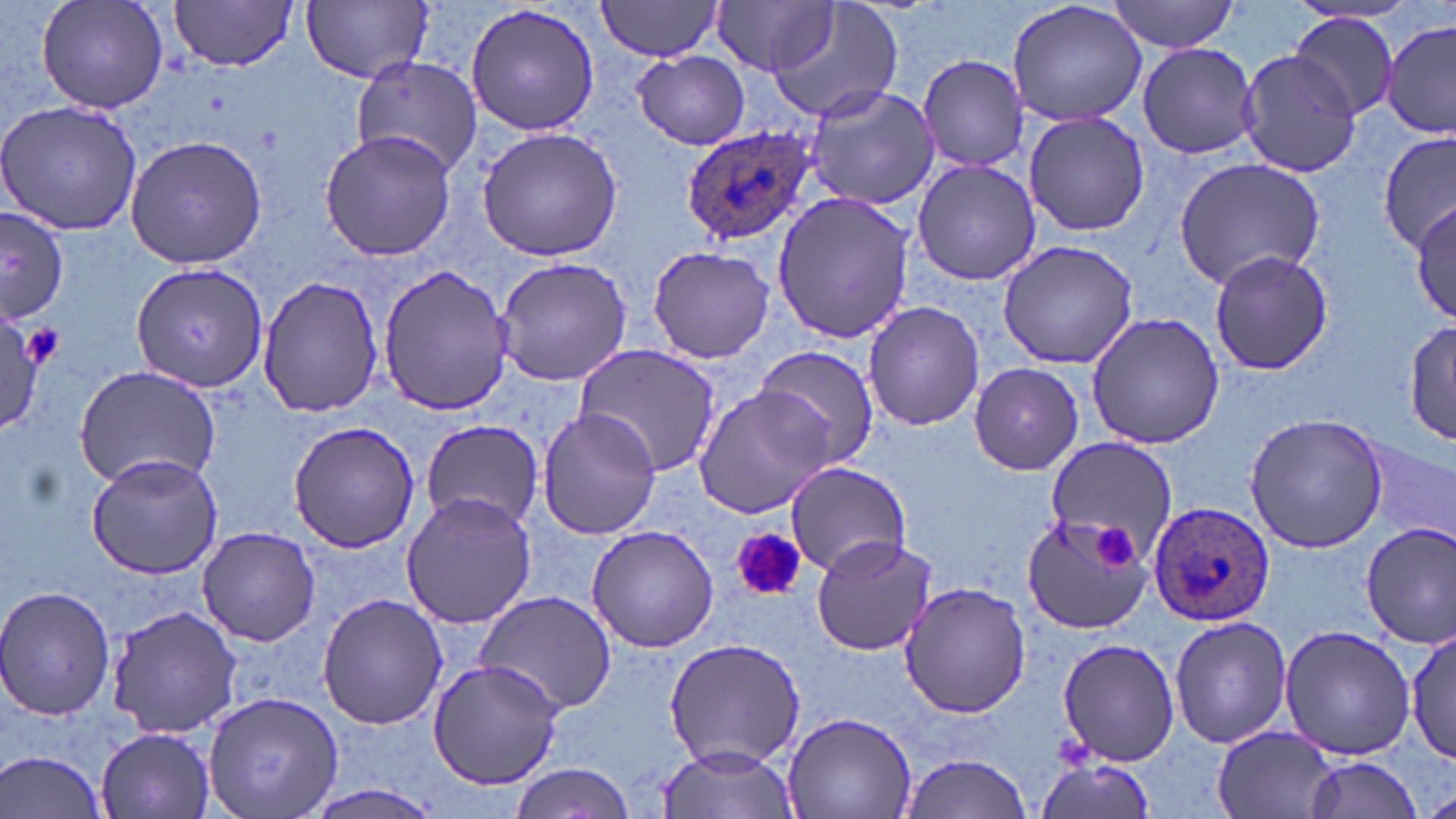
Summary:
  - Coordinate format: approximate bounding boxes as [x1, y1, x2, y2] in pixels
  - Platelet locations: [19, 323, 65, 371], [1095, 525, 1136, 567], [730, 528, 806, 601]
  - Plasmodium ovale-infected red blood cell locations: [682, 126, 814, 244], [1148, 503, 1277, 627]
  - Uninfected red blood cell locations: [35, 0, 169, 116], [301, 0, 433, 84], [714, 0, 839, 77], [1008, 0, 1149, 129], [168, 1, 299, 72], [597, 1, 727, 59], [764, 1, 905, 125], [1107, 1, 1241, 53], [466, 3, 600, 138], [1289, 12, 1399, 123], [1382, 20, 1456, 138], [1136, 41, 1259, 159], [634, 50, 750, 150], [1235, 50, 1361, 176], [918, 54, 1031, 172], [350, 56, 483, 179], [802, 84, 940, 210], [0, 99, 144, 238], [1024, 109, 1148, 238], [477, 127, 625, 262], [319, 130, 456, 263], [1378, 132, 1455, 252], [124, 133, 267, 269], [910, 157, 1040, 285], [1173, 158, 1326, 287], [771, 191, 916, 345], [1411, 201, 1456, 327], [0, 211, 71, 323], [995, 240, 1140, 369], [647, 245, 775, 365], [1207, 248, 1333, 376], [495, 255, 633, 386], [131, 263, 267, 395], [375, 263, 516, 418], [256, 273, 383, 419], [862, 301, 983, 431], [1085, 312, 1228, 450], [0, 313, 50, 430], [1404, 322, 1456, 446], [575, 346, 722, 476], [756, 346, 879, 469], [968, 362, 1085, 476], [74, 365, 223, 490], [693, 385, 837, 520], [535, 407, 661, 541], [1245, 410, 1391, 553], [287, 421, 420, 554], [419, 421, 542, 529], [1042, 437, 1175, 556], [1359, 439, 1454, 546], [85, 450, 225, 580], [784, 462, 913, 576], [398, 491, 538, 631], [1020, 513, 1152, 636], [1357, 521, 1456, 647], [585, 524, 718, 651], [197, 526, 320, 646], [810, 532, 939, 657], [899, 580, 1031, 720], [1, 587, 118, 721], [475, 590, 619, 717], [317, 593, 448, 731], [108, 605, 240, 738], [1170, 614, 1290, 749], [1278, 623, 1419, 760], [1409, 628, 1454, 763], [664, 637, 807, 769], [1057, 638, 1182, 767], [427, 659, 566, 790], [204, 690, 344, 819], [782, 710, 916, 819], [94, 725, 217, 819], [1214, 727, 1338, 818], [656, 744, 802, 819], [1, 749, 110, 819], [896, 752, 1034, 819], [1034, 755, 1160, 817], [1298, 756, 1428, 819], [506, 763, 633, 819], [299, 781, 448, 819]
  - Slide-level diagnosis: Plasmodium ovale
  - Field of view: one of a larger specimen
  - Image size: 1456×819 pixels
  - Preparation: thin blood smear
  - Modality: optical microscopy
  - Magnification: 1000x
  - Stain: May-Grünwald-Giemsa